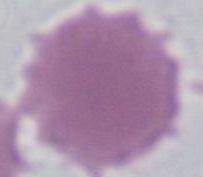 An erythrocyte is seen. Captured at 1000x magnification. Micrograph.